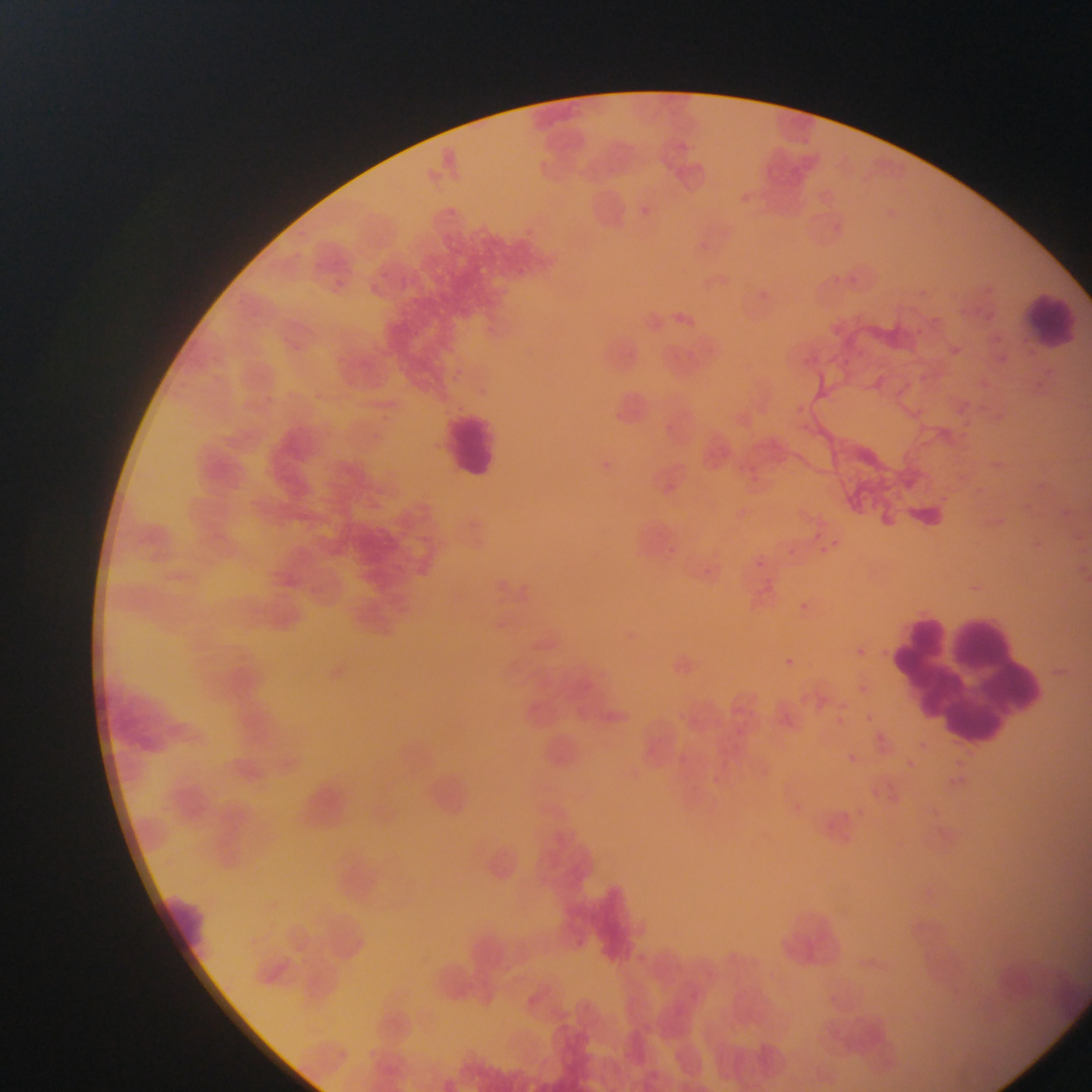

image_size: 1092×1092 pixels
plasmodium_parasite_locations: 'approximate bounding boxes as left top right bottom in pixels: 815 541 834 559; 750 554 768 572; 792 598 810 615; 778 653 799 673; 862 710 876 725; 845 751 859 764; 901 756 918 772; 942 770 968 793'
preparation: thin blood film
leukocyte_locations: 'approximate bounding boxes as left top right bottom in pixels: 1017 290 1086 354; 440 407 505 485; 883 599 1062 753; 159 887 213 946'
capture: mobile-phone photograph through a microscope
country: Ghana
field_of_view: single